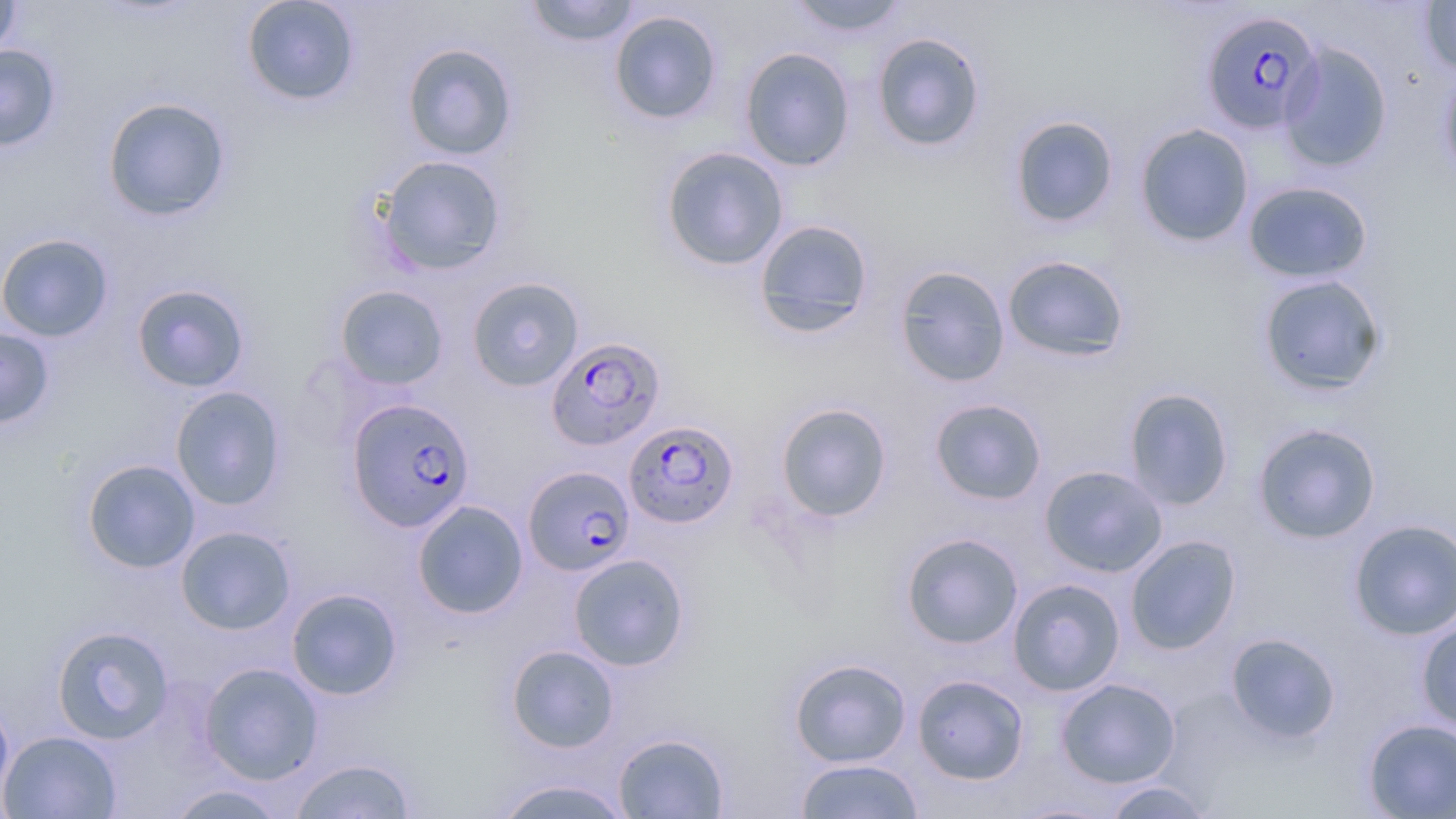

{
  "slide_level_diagnosis": "Plasmodium falciparum",
  "modality": "optical microscopy",
  "preparation": "thin blood film",
  "field_of_view": "single",
  "stain": "May-Grünwald-Giemsa",
  "plasmodium_falciparum_infected_red_blood_cell_locations": "approximate bounding boxes as named x1/y1/x2/y2 corners in pixels: (x1=1200, y1=10, x2=1325, y2=136), (x1=551, y1=340, x2=658, y2=448), (x1=347, y1=398, x2=475, y2=532), (x1=623, y1=420, x2=740, y2=529), (x1=524, y1=466, x2=635, y2=576)",
  "image_size": "1456×819 pixels",
  "magnification": "1000x",
  "uninfected_red_blood_cell_locations": "approximate bounding boxes as named x1/y1/x2/y2 corners in pixels: (x1=0, y1=0, x2=22, y2=59), (x1=241, y1=0, x2=361, y2=106), (x1=523, y1=0, x2=642, y2=47), (x1=786, y1=0, x2=911, y2=39), (x1=1418, y1=1, x2=1456, y2=75), (x1=608, y1=9, x2=723, y2=125), (x1=871, y1=32, x2=986, y2=152), (x1=1279, y1=41, x2=1393, y2=172), (x1=401, y1=42, x2=518, y2=161), (x1=0, y1=45, x2=62, y2=152), (x1=739, y1=47, x2=855, y2=171), (x1=1438, y1=66, x2=1456, y2=187), (x1=102, y1=97, x2=232, y2=222), (x1=1009, y1=115, x2=1119, y2=228), (x1=1135, y1=122, x2=1254, y2=248), (x1=659, y1=145, x2=790, y2=272), (x1=375, y1=154, x2=507, y2=276), (x1=1242, y1=180, x2=1374, y2=284), (x1=753, y1=219, x2=875, y2=337), (x1=0, y1=233, x2=115, y2=342), (x1=1002, y1=254, x2=1130, y2=362), (x1=894, y1=264, x2=1010, y2=388), (x1=1257, y1=274, x2=1388, y2=396), (x1=466, y1=276, x2=584, y2=392), (x1=131, y1=283, x2=250, y2=393), (x1=334, y1=285, x2=449, y2=390), (x1=0, y1=326, x2=55, y2=429), (x1=170, y1=385, x2=286, y2=510), (x1=1123, y1=387, x2=1235, y2=511), (x1=929, y1=397, x2=1047, y2=505), (x1=775, y1=402, x2=893, y2=523), (x1=1252, y1=422, x2=1382, y2=543), (x1=82, y1=459, x2=201, y2=574), (x1=1039, y1=465, x2=1168, y2=577), (x1=412, y1=500, x2=528, y2=619), (x1=1348, y1=518, x2=1456, y2=640), (x1=175, y1=526, x2=296, y2=635), (x1=901, y1=532, x2=1024, y2=649), (x1=1124, y1=534, x2=1242, y2=654), (x1=568, y1=554, x2=690, y2=671), (x1=1007, y1=578, x2=1125, y2=697), (x1=286, y1=587, x2=403, y2=701), (x1=1416, y1=617, x2=1456, y2=736), (x1=52, y1=625, x2=175, y2=745), (x1=1225, y1=632, x2=1342, y2=745), (x1=505, y1=644, x2=619, y2=753), (x1=789, y1=658, x2=912, y2=767), (x1=199, y1=662, x2=324, y2=784), (x1=912, y1=674, x2=1029, y2=785), (x1=1056, y1=678, x2=1181, y2=787), (x1=0, y1=693, x2=14, y2=810), (x1=1362, y1=718, x2=1456, y2=818), (x1=1, y1=730, x2=122, y2=818), (x1=613, y1=732, x2=729, y2=818), (x1=289, y1=758, x2=418, y2=818), (x1=793, y1=758, x2=925, y2=819), (x1=490, y1=777, x2=636, y2=818), (x1=1099, y1=781, x2=1215, y2=818), (x1=166, y1=783, x2=291, y2=819), (x1=1011, y1=801, x2=1117, y2=818)"
}